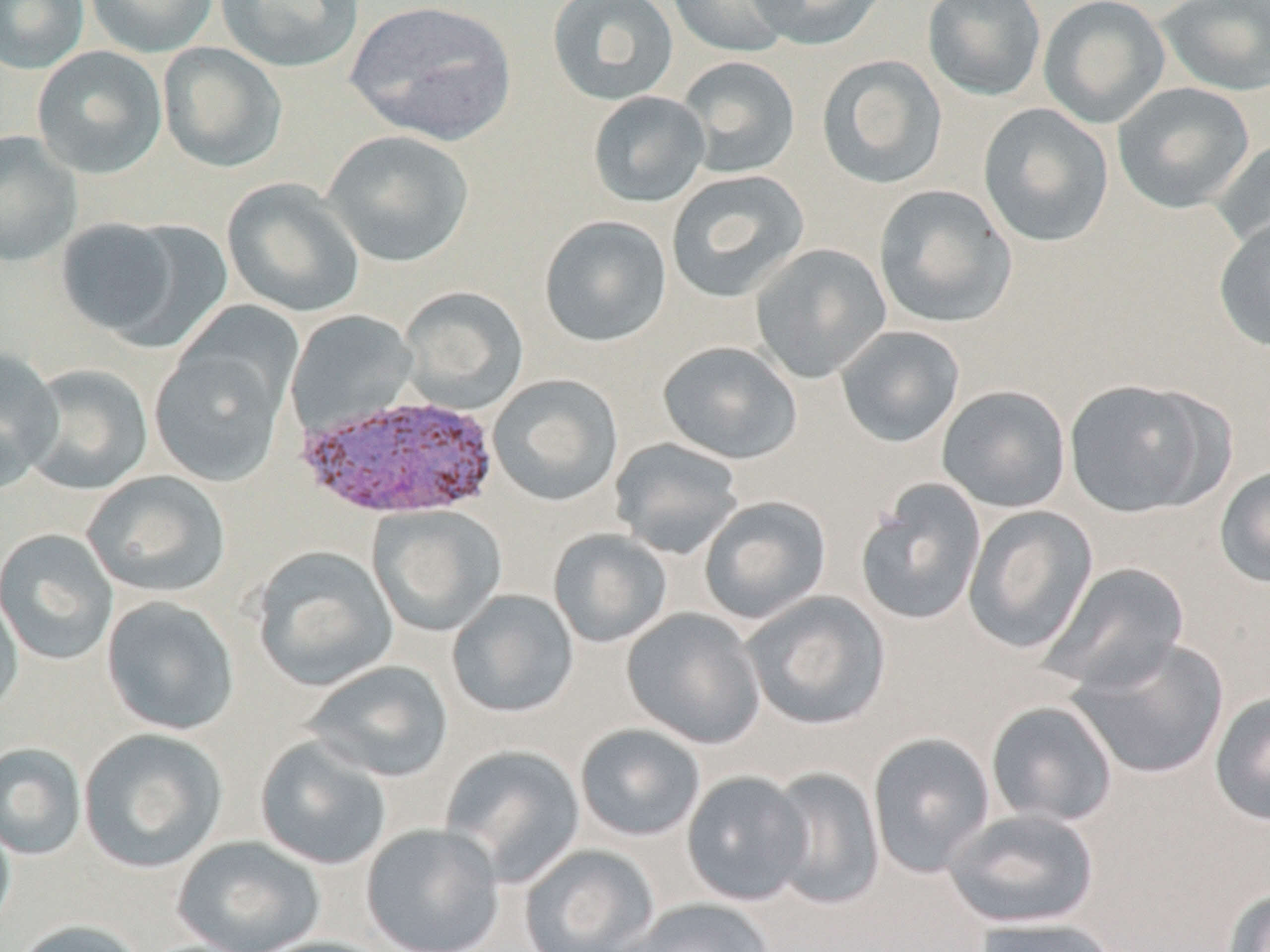
slide-level diagnosis = Plasmodium vivax
preparation = thin blood smear
stain = May-Grünwald-Giemsa
Plasmodium vivax-infected red blood cell locations = approximate bounding boxes as (x1,y1)-(x2,y2) corner pairs in pixels: (295,393)-(500,520)
modality = optical microscopy
field of view = single
uninfected red blood cell locations = approximate bounding boxes as (x1,y1)-(x2,y2) corner pairs in pixels: (1,0)-(89,74), (83,0)-(220,58), (215,0)-(364,73), (345,0)-(518,146), (546,0)-(679,106), (667,0)-(798,58), (745,0)-(890,50), (922,0)-(1047,102), (1038,0)-(1170,129), (1155,0)-(1270,97), (158,42)-(287,173), (32,46)-(167,179), (816,54)-(948,190), (676,56)-(800,180), (1112,82)-(1255,214), (587,91)-(710,208), (978,103)-(1114,248), (0,130)-(81,266), (322,130)-(474,268), (1210,138)-(1270,256), (665,169)-(810,302), (222,178)-(365,318), (873,184)-(1017,329), (539,215)-(672,347), (1213,215)-(1270,351), (55,216)-(199,344), (750,243)-(892,384), (398,286)-(529,415), (173,301)-(304,423), (285,310)-(419,436), (835,324)-(965,448), (657,341)-(802,465), (149,345)-(288,487), (0,348)-(64,490), (20,364)-(153,496), (488,374)-(624,507), (1063,377)-(1223,518), (937,385)-(1071,513), (609,437)-(744,559), (1214,465)-(1270,588), (82,471)-(231,599), (855,478)-(987,627), (698,495)-(832,624), (368,505)-(508,637), (962,505)-(1098,655), (548,528)-(672,648), (0,529)-(118,665), (251,546)-(398,692), (1041,562)-(1190,695), (0,586)-(23,723), (447,589)-(579,718), (742,591)-(892,731), (100,596)-(240,737), (621,608)-(766,749), (1069,637)-(1229,780), (302,660)-(454,783), (1209,690)-(1270,827), (986,700)-(1119,828), (573,724)-(706,842), (78,728)-(228,874), (867,732)-(996,878), (254,736)-(391,871), (0,743)-(87,860), (440,745)-(586,887), (764,766)-(886,910), (681,771)-(812,906), (942,808)-(1101,930), (0,813)-(15,936), (361,823)-(505,952), (172,836)-(325,952), (519,844)-(660,952), (1220,887)-(1270,952), (621,898)-(777,952), (972,916)-(1121,952), (12,919)-(147,952), (248,936)-(397,952)
image size = 1270×952 pixels
magnification = 1000x